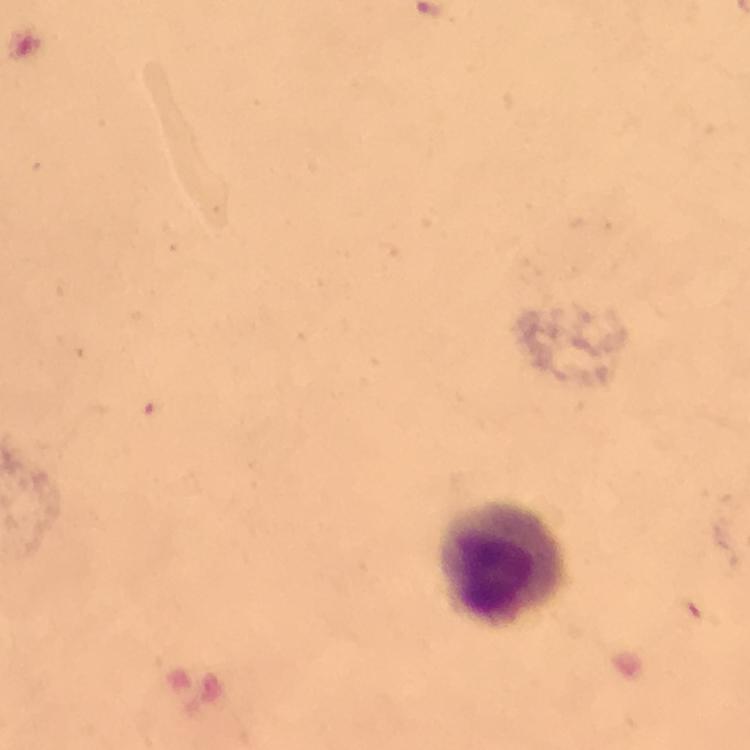
Approximate centers as {x, y} in pixels. Leukocyte locations: {504, 566}. From a malaria diagnostic workup. Image is 750×750 pixels. Malaria parasites: none seen. Cropped region of a single field of view. Immersion oil was used. Photographed through the microscope with a smartphone camera. At 100x magnification. Giemsa stain. Thick smear.